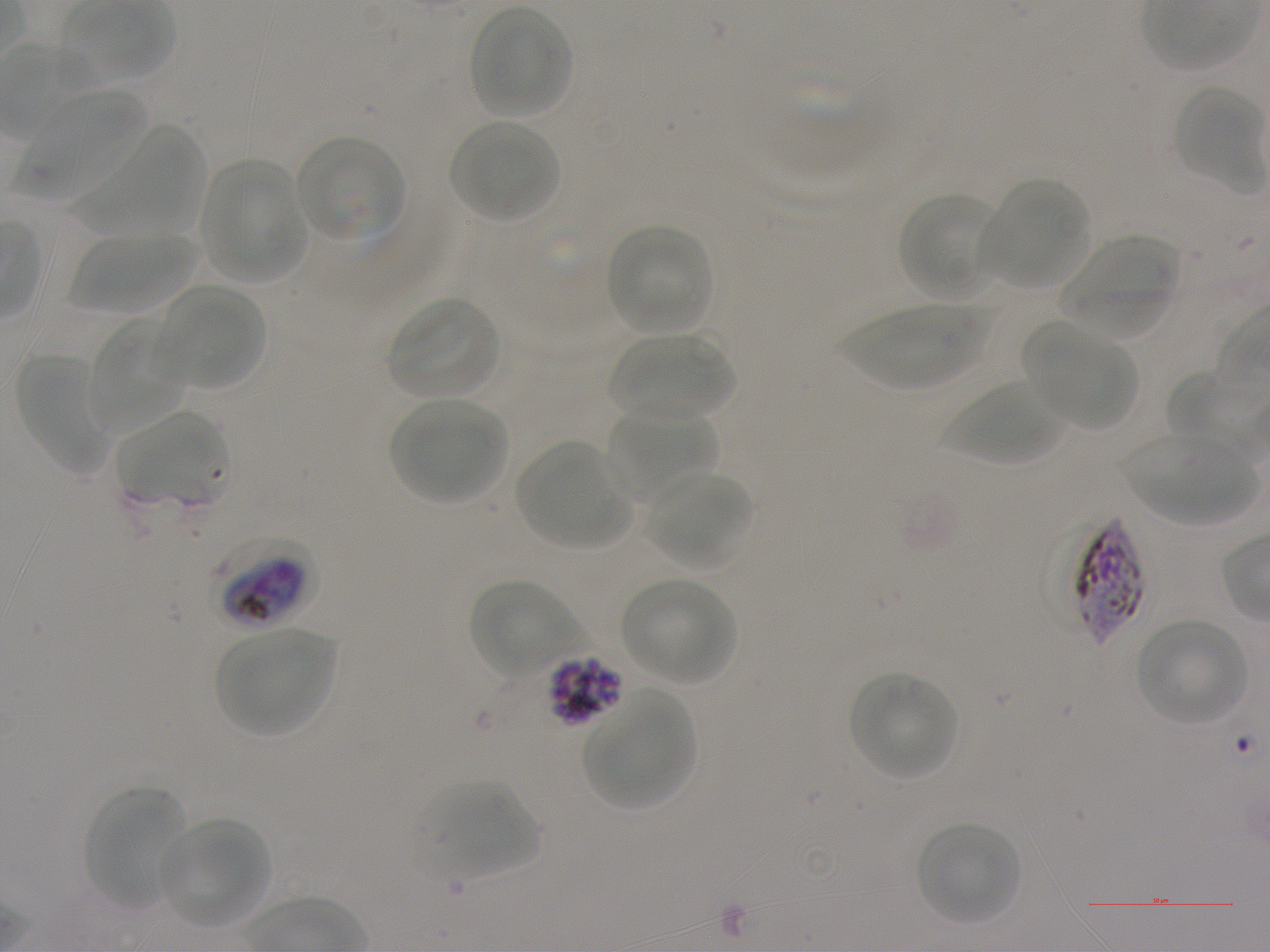
Not every red blood cell is marked. A life-cycle stage — or a range of stages, where the recorded stages span more than one — follows each staged infected red blood cell.
culture = in-vitro Plasmodium falciparum strain NF54, static
locations of uninfected red blood cells = approximate bounding rectangles given as corner coordinates in pixels from the top-left: (x1=468, y1=5, x2=574, y2=120), (x1=1173, y1=85, x2=1266, y2=189), (x1=19, y1=88, x2=149, y2=202), (x1=447, y1=119, x2=560, y2=222), (x1=79, y1=123, x2=205, y2=236), (x1=295, y1=134, x2=407, y2=242), (x1=203, y1=161, x2=306, y2=282), (x1=981, y1=180, x2=1090, y2=288), (x1=898, y1=192, x2=999, y2=298), (x1=605, y1=223, x2=713, y2=334), (x1=69, y1=232, x2=199, y2=313), (x1=1059, y1=238, x2=1183, y2=342), (x1=160, y1=285, x2=263, y2=388), (x1=386, y1=296, x2=502, y2=399), (x1=838, y1=304, x2=989, y2=390), (x1=86, y1=317, x2=187, y2=438), (x1=1025, y1=322, x2=1137, y2=430), (x1=609, y1=331, x2=737, y2=422), (x1=15, y1=353, x2=110, y2=477), (x1=1166, y1=369, x2=1246, y2=453), (x1=943, y1=380, x2=1065, y2=467), (x1=389, y1=398, x2=508, y2=503), (x1=607, y1=403, x2=719, y2=501), (x1=118, y1=410, x2=226, y2=504), (x1=1122, y1=433, x2=1258, y2=525), (x1=517, y1=443, x2=628, y2=546), (x1=646, y1=470, x2=752, y2=567), (x1=621, y1=577, x2=736, y2=685), (x1=469, y1=579, x2=580, y2=677), (x1=1136, y1=619, x2=1248, y2=726), (x1=216, y1=628, x2=334, y2=734), (x1=849, y1=672, x2=957, y2=779), (x1=584, y1=690, x2=694, y2=809), (x1=424, y1=782, x2=540, y2=879), (x1=85, y1=785, x2=189, y2=907), (x1=162, y1=817, x2=271, y2=926), (x1=915, y1=821, x2=1020, y2=925)
locations of red blood cells of indeterminate infection status = approximate bounding rectangles given as corner coordinates in pixels from the top-left: (x1=1074, y1=517, x2=1144, y2=646)
donor blood group = A+
stain = Giemsa
image size = 1270×952 pixels
preparation = thin blood smear
locations of infected red blood cells = approximate bounding rectangles given as corner coordinates in pixels from the top-left: (x1=217, y1=537, x2=318, y2=626) early trophozoite to late schizont; (x1=548, y1=653, x2=625, y2=725) schizont
objective = 100x, oil immersion, numerical aperture 1.25
field of view = one from this slide